Point out each leukocyte.
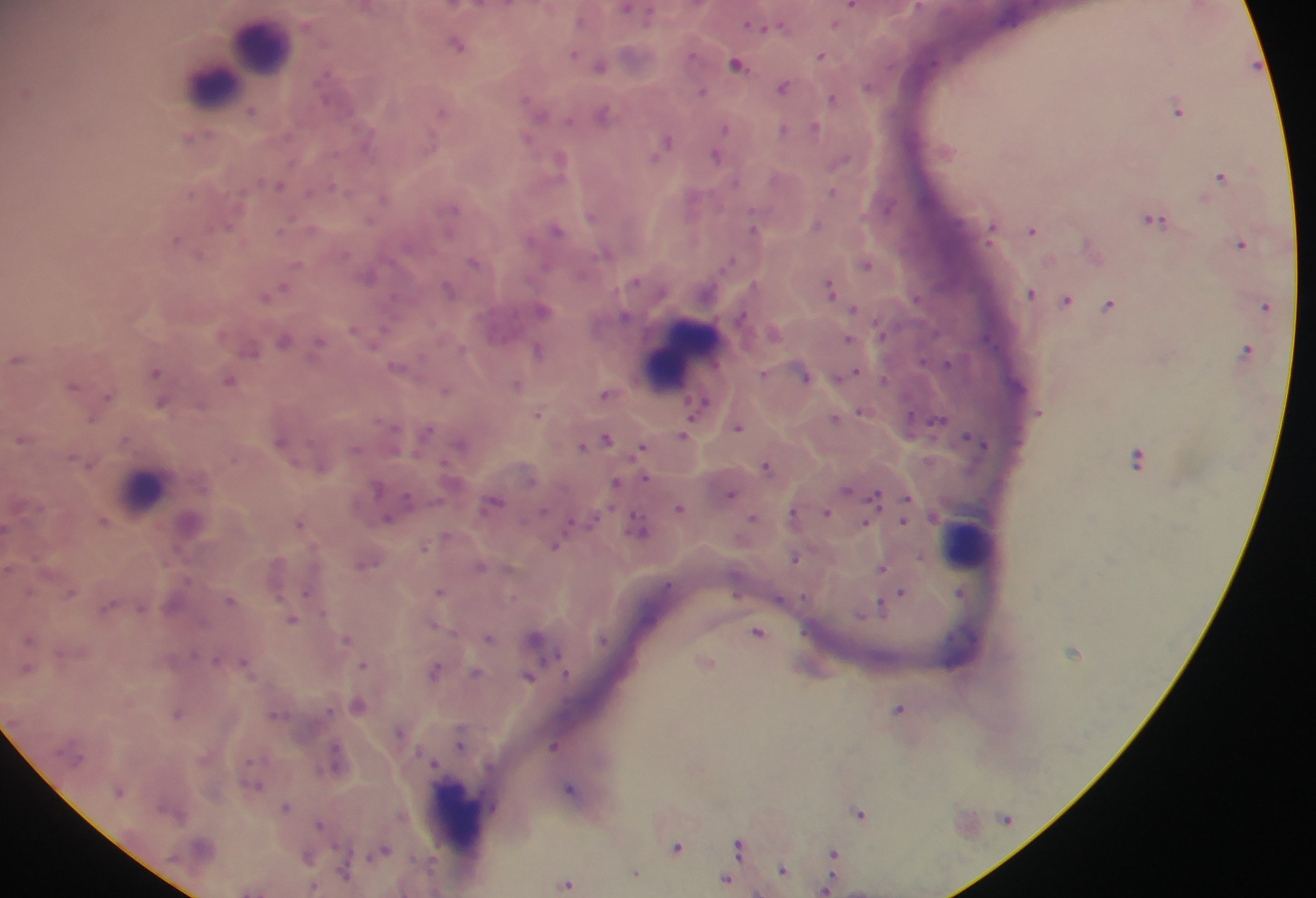
Approximate centers as {x, y} in pixels.
Leukocytes: {262, 41}, {244, 59}, {213, 81}, {681, 353}, {142, 490}, {966, 542}, {456, 818}.

Plasmodium parasite locations: {854, 5}, {765, 23}, {458, 42}, {821, 54}, {601, 63}, {737, 63}, {784, 85}, {702, 91}, {834, 96}, {1179, 107}, {604, 113}, {726, 127}, {784, 128}, {816, 128}, {192, 136}, {665, 142}, {717, 154}, {560, 159}, {1222, 175}, {280, 183}, {833, 189}, {1155, 217}, {817, 222}, {993, 225}, {555, 228}, {754, 228}, {1034, 229}, {177, 238}, {1242, 242}, {1093, 247}, {474, 260}, {867, 262}, {369, 274}, {831, 286}, {448, 289}, {273, 291}, {1032, 291}, {1067, 297}, {1110, 303}, {1266, 303}, {543, 308}, {855, 309}, {850, 338}, {285, 339}, {319, 343}, {1247, 348}, {252, 349}, {539, 349}, {17, 358}, {399, 367}, {157, 371}, {805, 373}, {850, 373}, {230, 378}, {517, 383}, {74, 384}, {446, 389}, {608, 392}, {108, 396}, {161, 401}, {699, 406}, {862, 411}, {539, 413}, {835, 417}, {738, 425}, {425, 433}, {685, 433}, {22, 437}, {607, 437}, {978, 439}, {282, 440}, {461, 442}, {585, 444}, {642, 447}, {1139, 457}, {767, 464}, {617, 482}, {846, 490}, {731, 492}, {877, 495}, {907, 498}, {494, 501}, {680, 507}, {827, 512}, {794, 514}, {389, 516}, {753, 518}, {903, 519}, {104, 520}, {300, 522}, {865, 522}, {641, 527}, {447, 536}, {556, 543}, {424, 547}, {795, 557}, {366, 562}, {481, 564}, {883, 566}, {441, 590}, {902, 592}, {961, 592}, {231, 599}, {896, 599}, {108, 606}, {882, 606}, {864, 613}, {292, 618}, {436, 626}, {759, 631}, {490, 635}, {347, 637}, {536, 638}, {706, 661}, {364, 664}, {436, 669}, {476, 673}, {529, 675}, {359, 704}, {900, 709}, {178, 713}, {402, 732}, {461, 743}, {556, 743}, {336, 760}, {254, 783}, {572, 788}, {120, 789}, {286, 806}, {860, 813}, {321, 823}, {741, 844}, {678, 847}, {383, 849}, {835, 854}, {309, 855}, {784, 868}, {346, 872}, {637, 872}, {726, 879}, {568, 883}, {827, 886}, {312, 888}. Single field of view. Image is 1316×898 pixels. Sample from Ghana. Photographed through a microscope with a mobile-phone camera. Thick blood film.